Classify this cell by malaria status.
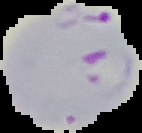

Parasitized.

From a thin blood film. Image is 142×133 pixels. Segmented cell region on a black background.